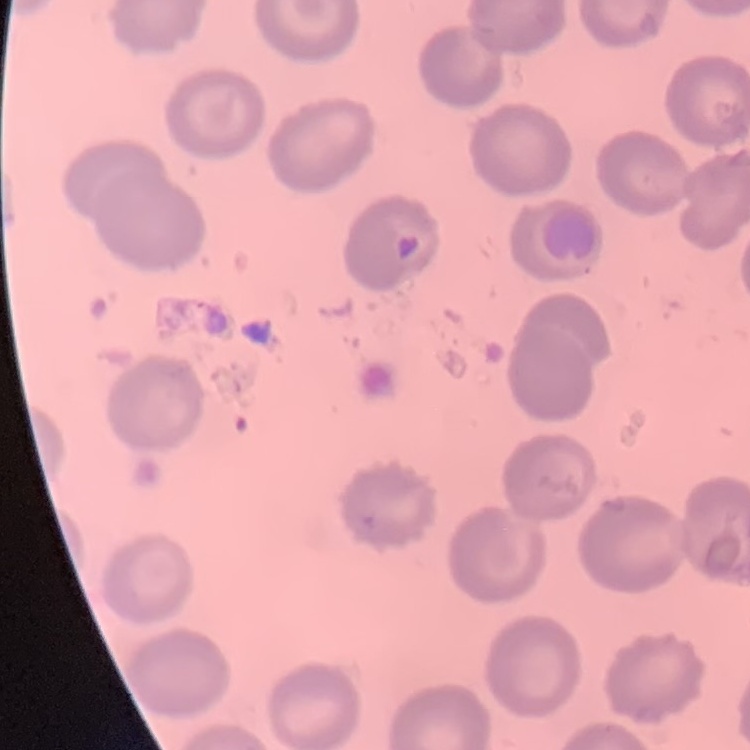

Summary:
  - Erythrocyte morphology: no rouleaux formation
  - Stain: Field's or Giemsa
  - Preparation: thin blood smear
  - Image type: one tile cut from a larger photomicrograph